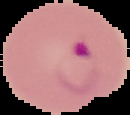

image type = segmented cell region on a black background
preparation = thin blood smear
image size = 130×115 pixels
result = malaria parasites detected